Locate every blood parasite and identify its species.
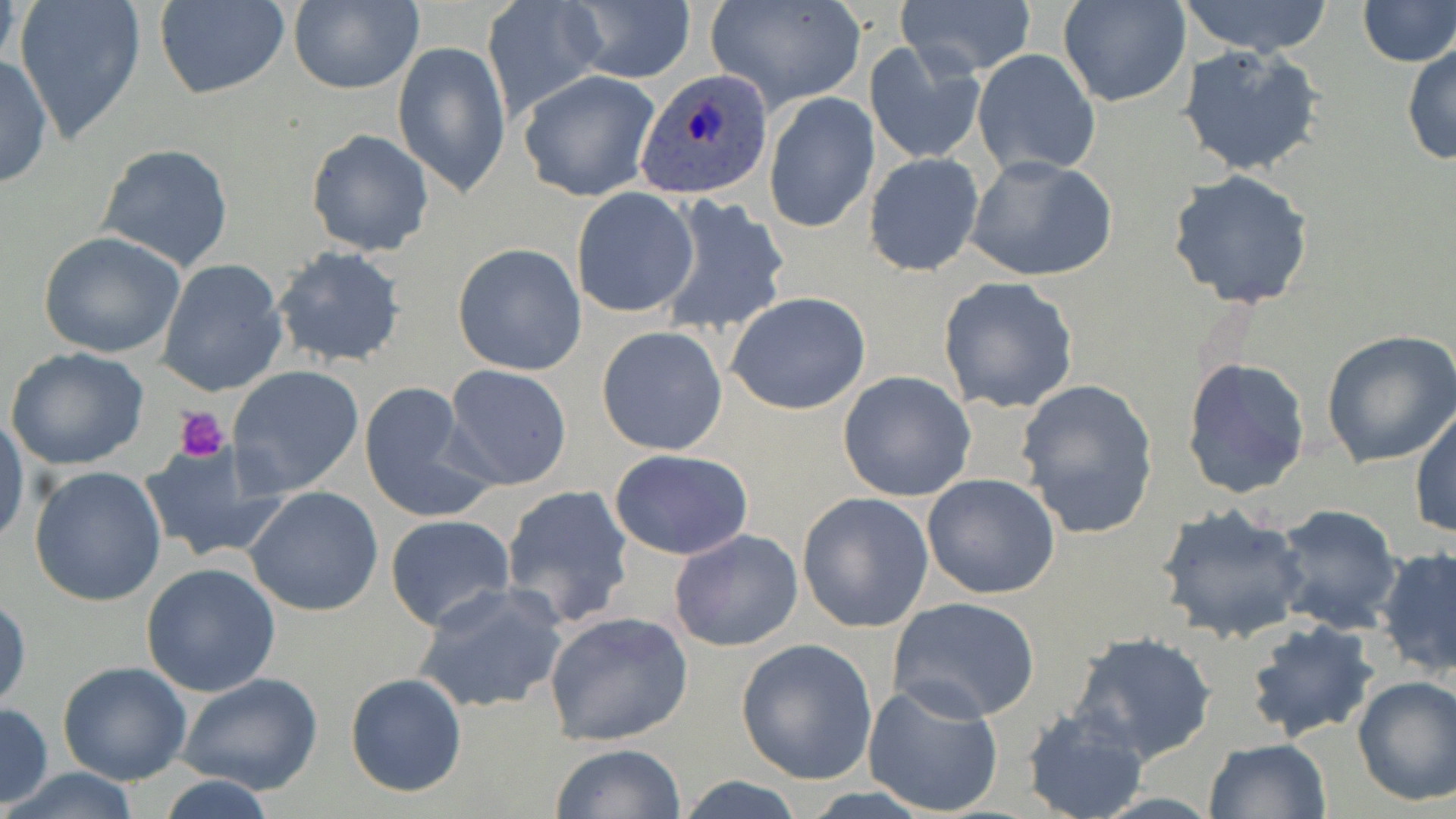
Approximate bounding boxes as [x1, y1, x2, y2] in pixels.
Plasmodium ovale-infected red blood cells: [638, 69, 771, 200].
No Plasmodium falciparum, Plasmodium malariae, Plasmodium vivax, Babesia divergens, or Trypanosoma brucei observed.

Platelet locations: [174, 407, 230, 461]. Uninfected red blood cell locations: [152, 0, 291, 100], [287, 0, 423, 95], [1058, 0, 1190, 107], [1179, 0, 1335, 55], [1356, 0, 1454, 67], [14, 1, 147, 142], [484, 1, 606, 120], [564, 1, 696, 84], [898, 1, 1036, 79], [707, 2, 866, 112], [393, 39, 510, 198], [866, 40, 986, 166], [1402, 40, 1455, 167], [1178, 41, 1325, 177], [973, 49, 1101, 178], [0, 55, 52, 191], [518, 70, 661, 201], [763, 93, 879, 234], [306, 128, 435, 257], [96, 143, 234, 271], [865, 153, 985, 276], [965, 156, 1118, 282], [1167, 169, 1315, 310], [571, 188, 699, 317], [656, 194, 792, 338], [38, 230, 187, 359], [452, 243, 587, 377], [270, 245, 408, 369], [156, 258, 290, 398], [937, 277, 1079, 414], [727, 292, 872, 416], [596, 326, 729, 454], [1321, 327, 1456, 469], [5, 345, 150, 471], [1182, 358, 1310, 498], [228, 364, 365, 498], [442, 365, 574, 491], [838, 371, 978, 502], [1015, 377, 1160, 539], [357, 381, 492, 523], [1410, 405, 1455, 540], [0, 414, 29, 549], [140, 442, 289, 563], [609, 449, 754, 561], [28, 465, 168, 606], [921, 474, 1061, 598], [501, 483, 636, 629], [244, 486, 383, 616], [796, 493, 934, 633], [1271, 504, 1401, 634], [1154, 505, 1309, 646], [384, 515, 516, 632], [668, 528, 804, 653], [1376, 545, 1456, 678], [139, 563, 282, 699], [413, 584, 569, 714], [0, 593, 30, 712], [886, 596, 1042, 723], [544, 610, 695, 746], [1244, 618, 1379, 745], [1066, 631, 1218, 764], [735, 638, 879, 785], [58, 661, 192, 786], [175, 672, 325, 795], [344, 672, 469, 796], [1352, 675, 1456, 806], [863, 680, 1006, 816], [0, 702, 53, 810], [1020, 705, 1151, 819], [1202, 738, 1331, 818], [549, 743, 687, 819], [6, 767, 143, 819], [149, 775, 284, 819], [676, 775, 808, 818]. Slide-level diagnosis: Plasmodium ovale. One field of a larger specimen. 1000x magnification. Optical microscopy. May-Grünwald-Giemsa-stained preparation. Thin blood smear. Image is 1456×819 pixels.